Describe the morphology of the erythrocytes.
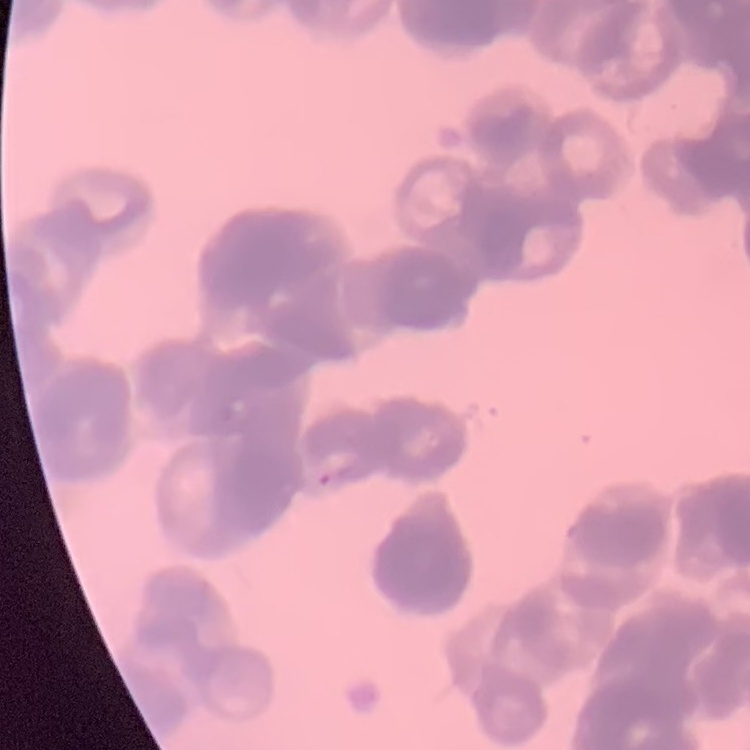
They show rouleaux formation.

image_type: square crop of a larger photomicrograph
preparation: thin blood smear
stain: Field's or Giemsa